Name the parasite shown.
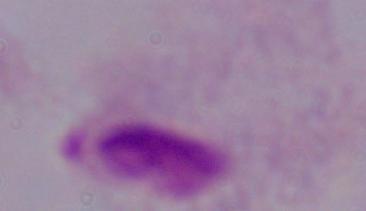

A trichomonad.

magnification: 1000x
modality: photomicrograph